Name the blood parasite species.
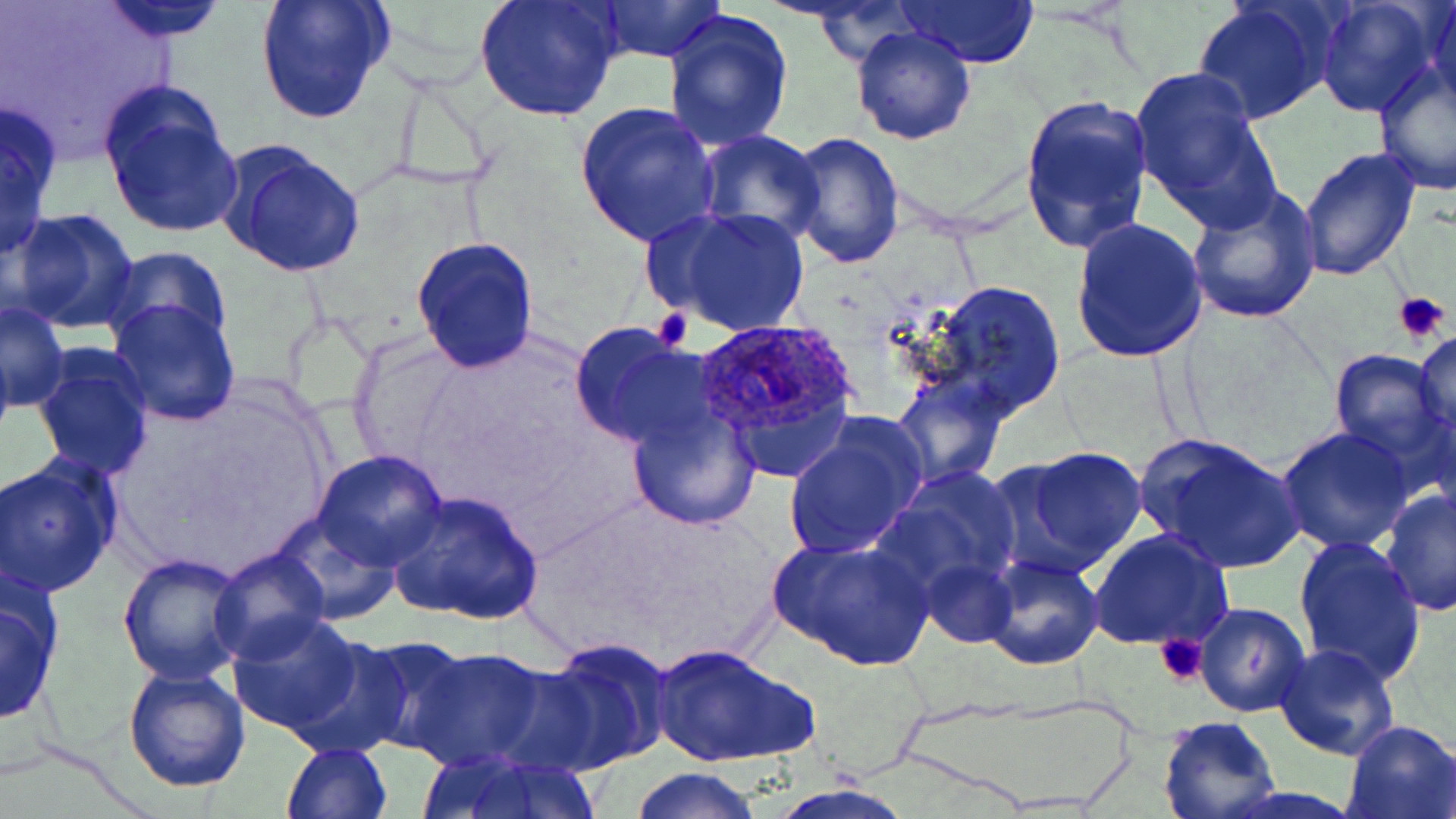

Plasmodium ovale.

field of view = single
magnification = 1000x
modality = light microscopy
uninfected red blood cell locations = approximate bounding boxes as [x1, y1, x2, y2] in pixels: [94, 0, 233, 42], [254, 0, 395, 125], [474, 0, 626, 124], [593, 0, 728, 62], [1313, 0, 1445, 120], [1426, 0, 1456, 119], [898, 1, 1042, 68], [1192, 2, 1332, 124], [817, 3, 921, 68], [663, 8, 795, 150], [851, 26, 977, 146], [1373, 61, 1456, 196], [1130, 64, 1275, 222], [99, 86, 245, 241], [1017, 94, 1154, 254], [0, 100, 65, 258], [573, 102, 720, 251], [695, 130, 824, 244], [786, 130, 904, 267], [216, 143, 367, 278], [1295, 148, 1421, 284], [1184, 183, 1321, 323], [647, 204, 811, 337], [8, 208, 140, 333], [1071, 215, 1208, 363], [411, 236, 541, 375], [100, 246, 232, 350], [924, 279, 1067, 419], [107, 298, 241, 426], [1, 302, 70, 413], [40, 310, 226, 460], [567, 322, 706, 450], [1412, 328, 1456, 447], [0, 331, 16, 451], [1328, 345, 1454, 470], [33, 346, 154, 481], [889, 373, 1009, 488], [624, 400, 761, 530], [782, 415, 929, 559], [1277, 427, 1418, 554], [1137, 433, 1306, 575], [991, 446, 1149, 579], [313, 453, 448, 570], [1, 456, 124, 598], [873, 465, 1023, 600], [1378, 486, 1455, 618], [386, 490, 544, 625], [270, 511, 400, 624], [1088, 528, 1234, 651], [769, 533, 932, 672], [1294, 535, 1426, 689], [207, 547, 328, 665], [117, 553, 249, 687], [982, 556, 1104, 671], [921, 558, 1016, 648], [0, 586, 61, 726], [1193, 603, 1309, 717], [225, 613, 366, 737], [285, 635, 415, 757], [356, 637, 477, 755], [532, 637, 673, 773], [649, 641, 816, 770], [1274, 643, 1401, 763], [406, 646, 554, 772], [123, 664, 252, 792], [1158, 715, 1282, 819], [1340, 718, 1456, 819], [281, 742, 393, 819], [426, 754, 603, 819], [628, 766, 763, 819]
Plasmodium ovale-infected red blood cell locations = approximate bounding boxes as [x1, y1, x2, y2] in pixels: [693, 319, 860, 462]
stain = May-Grünwald-Giemsa
preparation = thin blood film
image size = 1456×819 pixels
platelet locations = approximate bounding boxes as [x1, y1, x2, y2] in pixels: [1392, 288, 1453, 344], [652, 306, 692, 353], [1156, 633, 1211, 686]